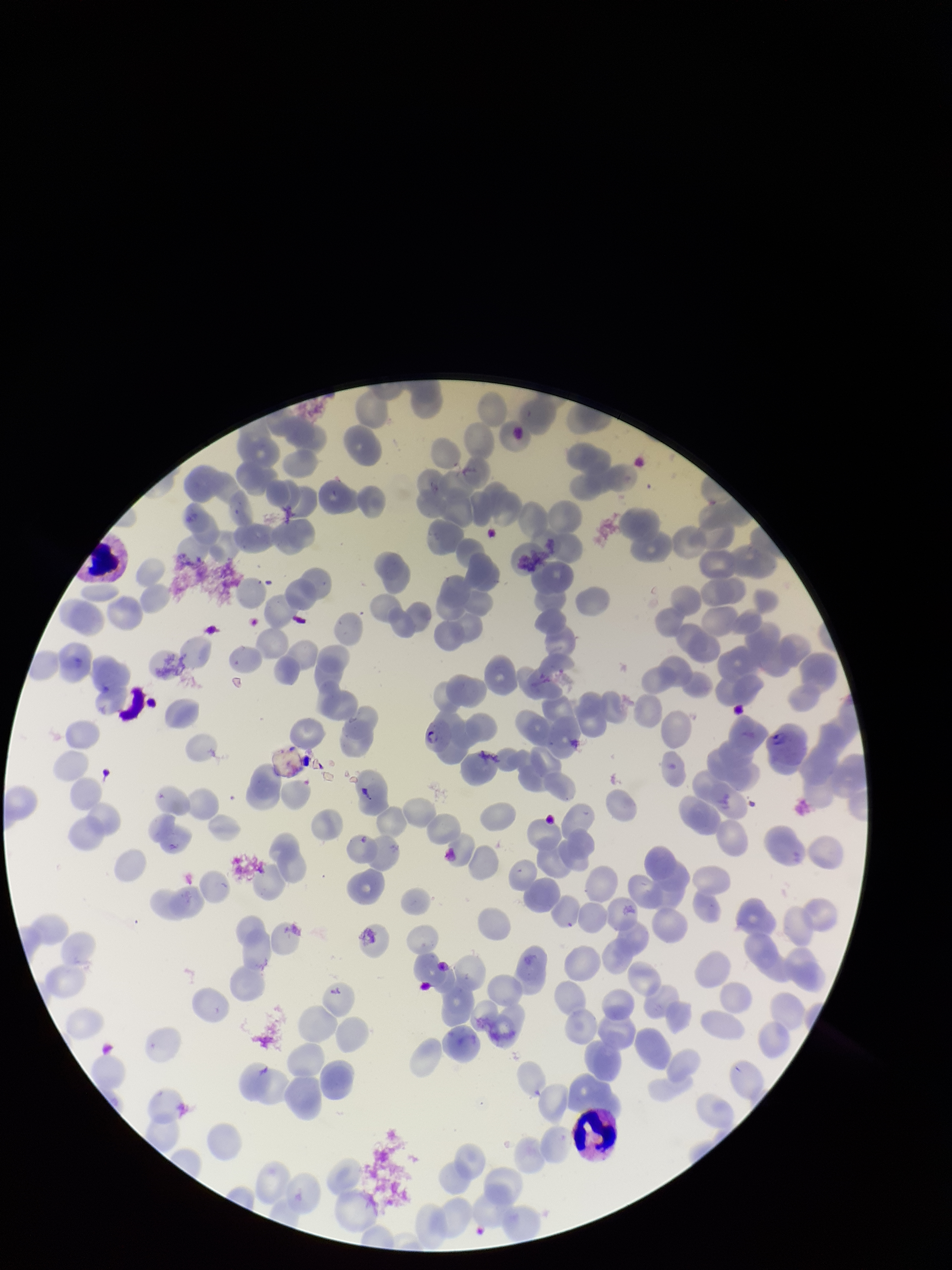

Summary:
  - Parasitized red blood cell count: 0
  - Preparation: thin
  - Patient malaria status: infected
  - Parasitized red blood cells: none identified
  - Species reported for this patient: Plasmodium falciparum
  - Stain: Giemsa
  - Image size: 952×1270 pixels
  - Red blood cell count: 155
  - Field of view: single
  - Capture: smartphone photograph through the microscope eyepiece